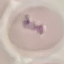

Malaria status: uninfected. Thin blood film. Giemsa stain. Cell patch, automatically extracted from a larger field of view and resized to 64 × 64 pixels. Photographed with a smartphone camera at the microscope eyepiece.